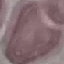 Result: no malaria parasites detected. Photographed with a smartphone camera at the microscope eyepiece. Giemsa-stained preparation. Thin smear of blood. Automatically extracted cell patch, resized to 64 × 64 pixels.